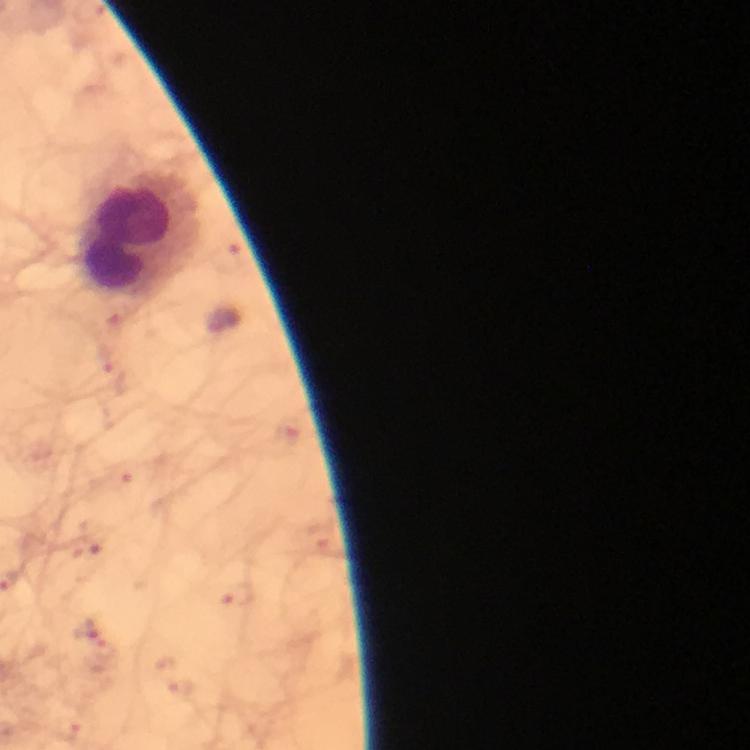
Approximate centers as [x, y] in pixels.
Summary:
  - Malaria parasite locations: [223, 321]
  - Leukocyte locations: [135, 242]
  - Context: from a diagnostic examination for malaria
  - Magnification: 100x
  - Immersion oil: used
  - Stain: Giemsa
  - Capture: smartphone camera through the microscope
  - Preparation: thick blood film
  - Cropped from: one field of view
  - Image size: 750×750 pixels